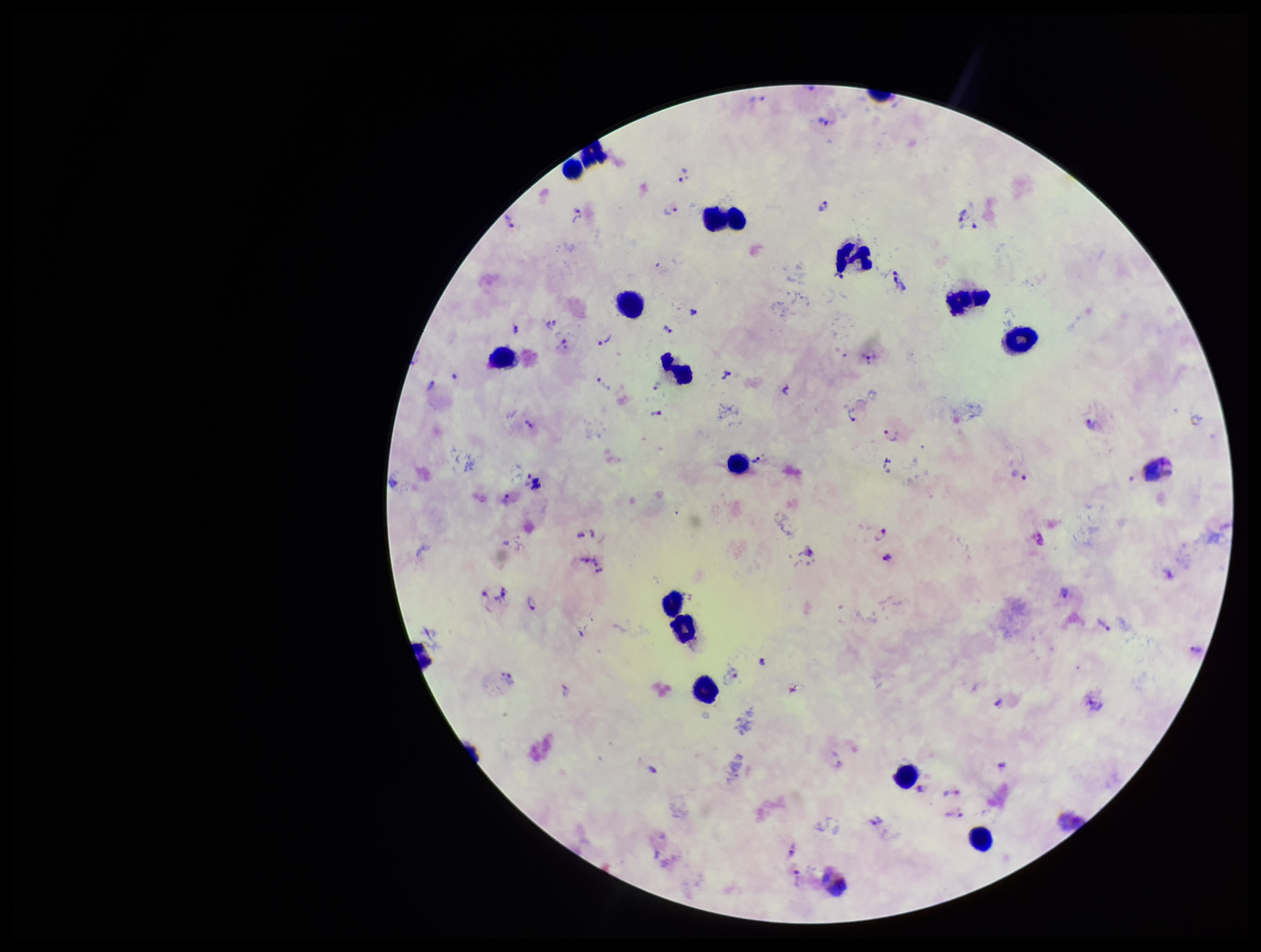

Summary:
  - Patient malaria status: infected
  - Plasmodium parasites: seen
  - Image size: 1261×952 pixels
  - Preparation: thick
  - Leukocyte count: 17
  - Parasite count: 52
  - Stain: Giemsa
  - Species reported for this patient: Plasmodium vivax
  - Field of view: single
  - Capture: smartphone photograph through the microscope eyepiece